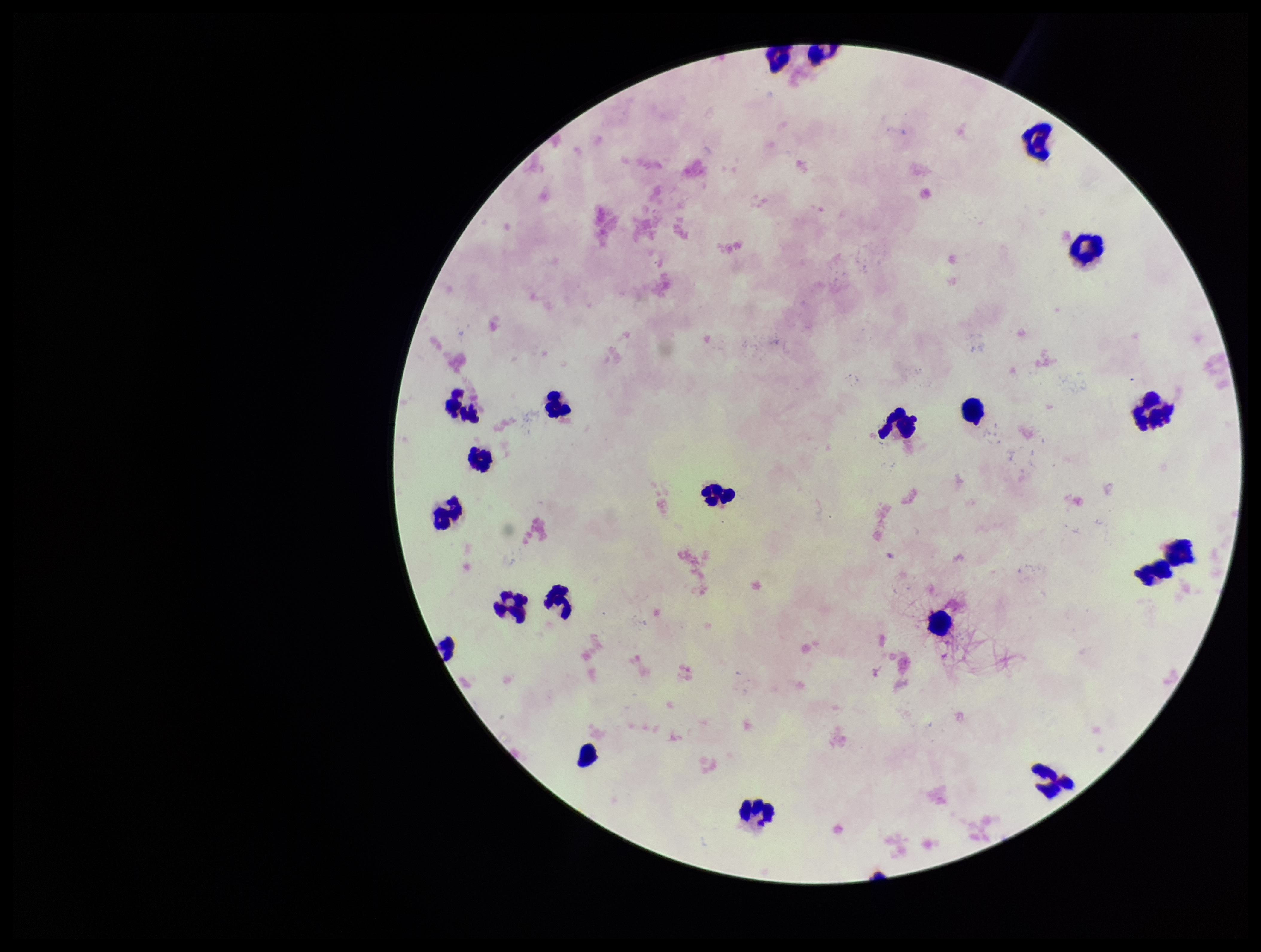
Smartphone photograph taken through the eyepiece of a microscope. Plasmodium parasites: none detected. Image is 1261×952 pixels. One field from this slide. Parasite count: 0. Preparation: thick blood smear. Leukocyte count: 21. Giemsa stain. Patient malaria status: negative.